Name the parasite shown.
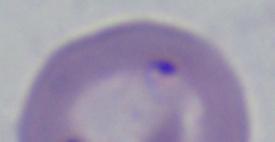

Babesia.

magnification: 1000x
modality: photomicrograph